Identify the parasite.
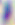

Toxoplasma gondii.

Micrograph. Captured at 400x magnification.